Evaluate for malaria.
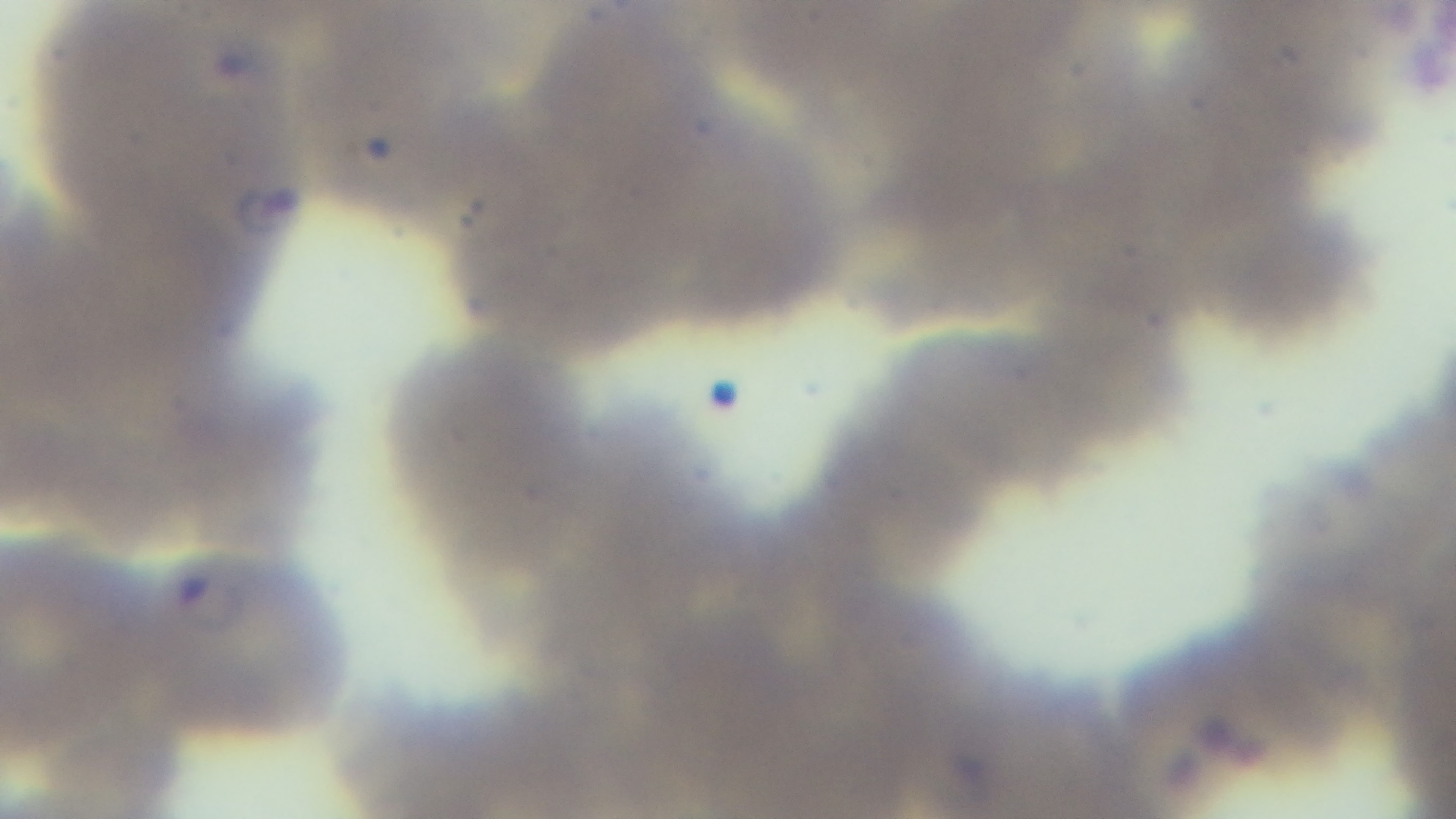
Infected.

Giemsa-stained. Preparation: thin smear. 100x oil-immersion objective. Captured with a mounted 4K digital camera. Photomicrograph. Single field of view.